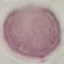

Summary:
  - Result: negative for malaria parasites
  - Preparation: thin blood smear
  - Capture: smartphone through the microscope eyepiece
  - Image type: automatically extracted cell patch, resized to 64 × 64 pixels
  - Stain: Giemsa